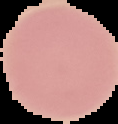

Image is 118×124 pixels. From a thin blood smear. The area outside the segmented cell region is set to black. Result: no Plasmodium parasites detected.